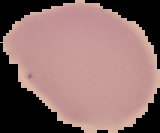
image size = 160×133 pixels
preparation = thin blood smear
image type = cell region segmented out of the field of view; surrounding area masked to black
malaria status = uninfected